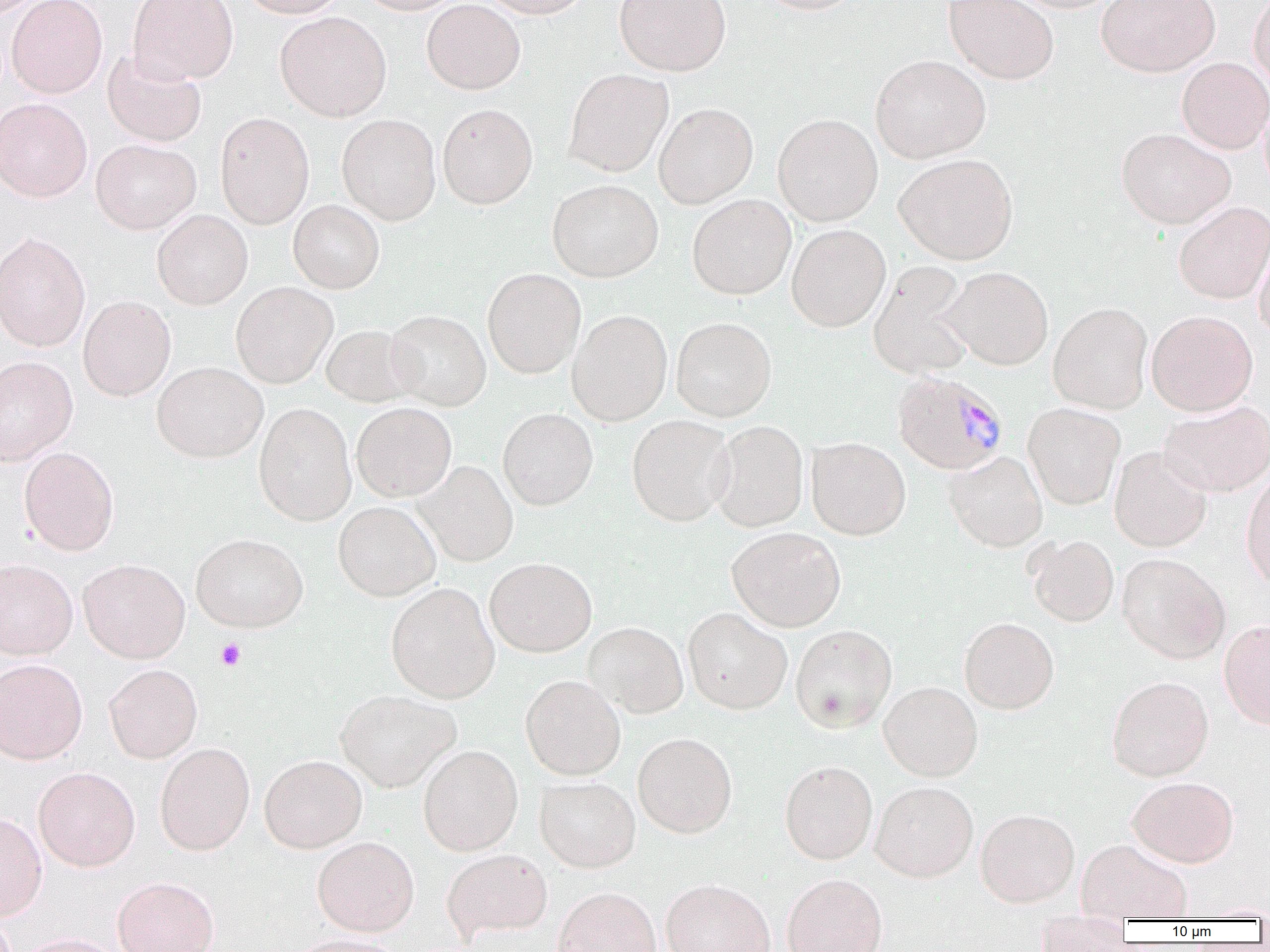

slide-level diagnosis = Plasmodium malariae
image size = 1270×952 pixels
uninfected red blood cell locations = approximate bounding boxes as (x1, y1, x2, y2) in pixels: (0, 0, 46, 20), (6, 0, 107, 99), (127, 0, 239, 84), (237, 0, 347, 18), (353, 0, 467, 15), (421, 0, 525, 94), (479, 0, 593, 19), (613, 0, 731, 76), (754, 0, 866, 14), (943, 0, 1059, 85), (1005, 0, 1123, 13), (1096, 0, 1220, 77), (1248, 0, 1270, 94), (428, 1, 529, 208), (275, 11, 392, 122), (101, 49, 207, 147), (870, 54, 991, 164), (1177, 57, 1270, 154), (563, 68, 673, 177), (0, 98, 92, 202), (436, 103, 538, 209), (653, 103, 758, 208), (214, 112, 314, 229), (772, 113, 883, 226), (336, 114, 441, 225), (1116, 127, 1236, 229), (90, 138, 201, 234), (894, 153, 1018, 265), (547, 179, 664, 282), (687, 194, 796, 300), (288, 200, 385, 293), (1173, 201, 1270, 304), (152, 209, 253, 310), (786, 224, 891, 332), (0, 231, 91, 352), (1254, 233, 1270, 344), (868, 261, 977, 380), (943, 266, 1054, 370), (482, 268, 586, 378), (230, 282, 337, 388), (78, 296, 175, 401), (1048, 302, 1153, 414), (386, 310, 491, 411), (567, 310, 673, 425), (1146, 310, 1258, 416), (671, 317, 776, 421), (321, 324, 418, 407), (0, 356, 78, 465), (151, 361, 268, 462), (1158, 401, 1270, 497), (254, 403, 357, 526), (351, 403, 457, 501), (1023, 403, 1125, 510), (498, 408, 598, 510), (626, 414, 735, 526), (709, 420, 809, 532), (806, 437, 910, 540), (18, 446, 119, 556), (1109, 447, 1212, 552), (944, 451, 1048, 552), (413, 461, 518, 566), (1240, 473, 1270, 590), (333, 501, 440, 601), (726, 527, 846, 632), (190, 533, 308, 632), (1026, 535, 1119, 626), (1116, 553, 1230, 664), (485, 557, 597, 657), (77, 558, 190, 663), (0, 559, 77, 659), (385, 582, 500, 702), (683, 607, 792, 715), (959, 617, 1059, 714), (1219, 619, 1270, 729), (582, 622, 689, 718), (790, 624, 897, 733), (0, 658, 88, 764), (104, 664, 203, 763), (520, 674, 626, 780), (1107, 675, 1214, 781), (878, 681, 983, 781), (335, 690, 461, 791), (633, 731, 738, 838), (155, 743, 255, 855), (418, 744, 523, 856), (259, 754, 367, 853), (780, 760, 877, 864), (33, 767, 140, 871), (1127, 776, 1239, 867), (534, 777, 641, 872), (870, 780, 978, 882), (975, 808, 1080, 907), (0, 813, 47, 920), (312, 836, 419, 936), (1076, 838, 1192, 920), (442, 848, 553, 940), (782, 873, 887, 952), (112, 876, 219, 952), (661, 878, 775, 952), (552, 886, 661, 952), (1034, 917, 1131, 952), (13, 933, 124, 952), (290, 933, 407, 952)
magnification = 1000x
modality = light microscopy
platelet locations = approximate bounding boxes as (x1, y1, x2, y2) in pixels: (215, 638, 246, 671)
preparation = thin blood film
Plasmodium malariae-infected red blood cell locations = approximate bounding boxes as (x1, y1, x2, y2) in pixels: (892, 371, 1008, 475)
field of view = single